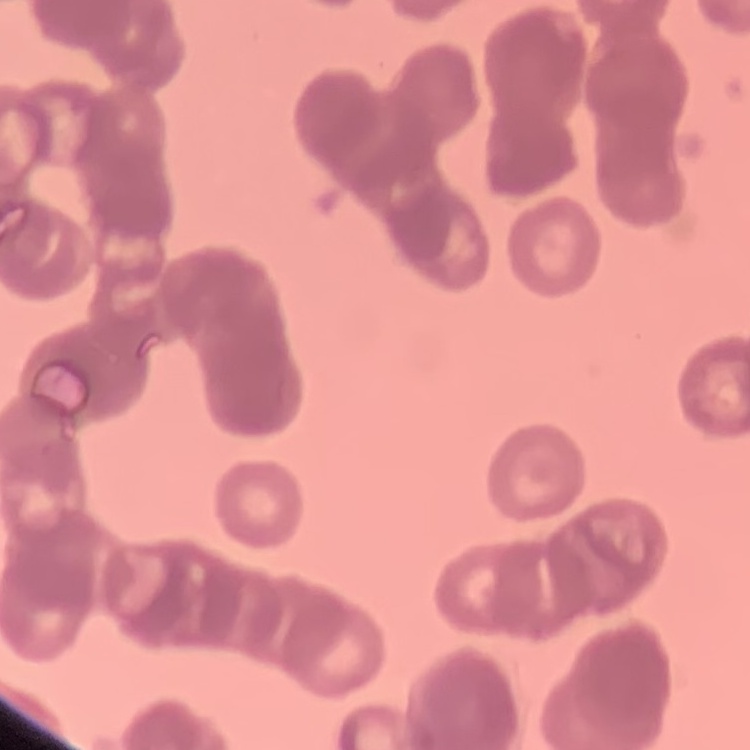 The red blood cells exhibit rouleaux formation. Thin blood smear. Stained with either Field's or Giemsa. One tile cut from a larger photomicrograph.